Report the malaria status of this cell.
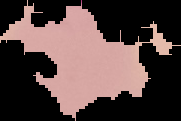

Parasitized.

Cell region segmented out of the field of view; the surrounding area is masked to black. From a thin blood film. Image is 181×121 pixels.